Name the cell type shown.
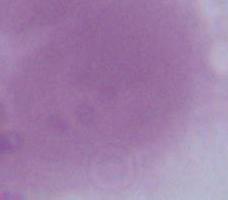

An erythrocyte.

Summary:
  - Modality: photomicrograph
  - Magnification: 1000x